Outline each blood parasite and name the species.
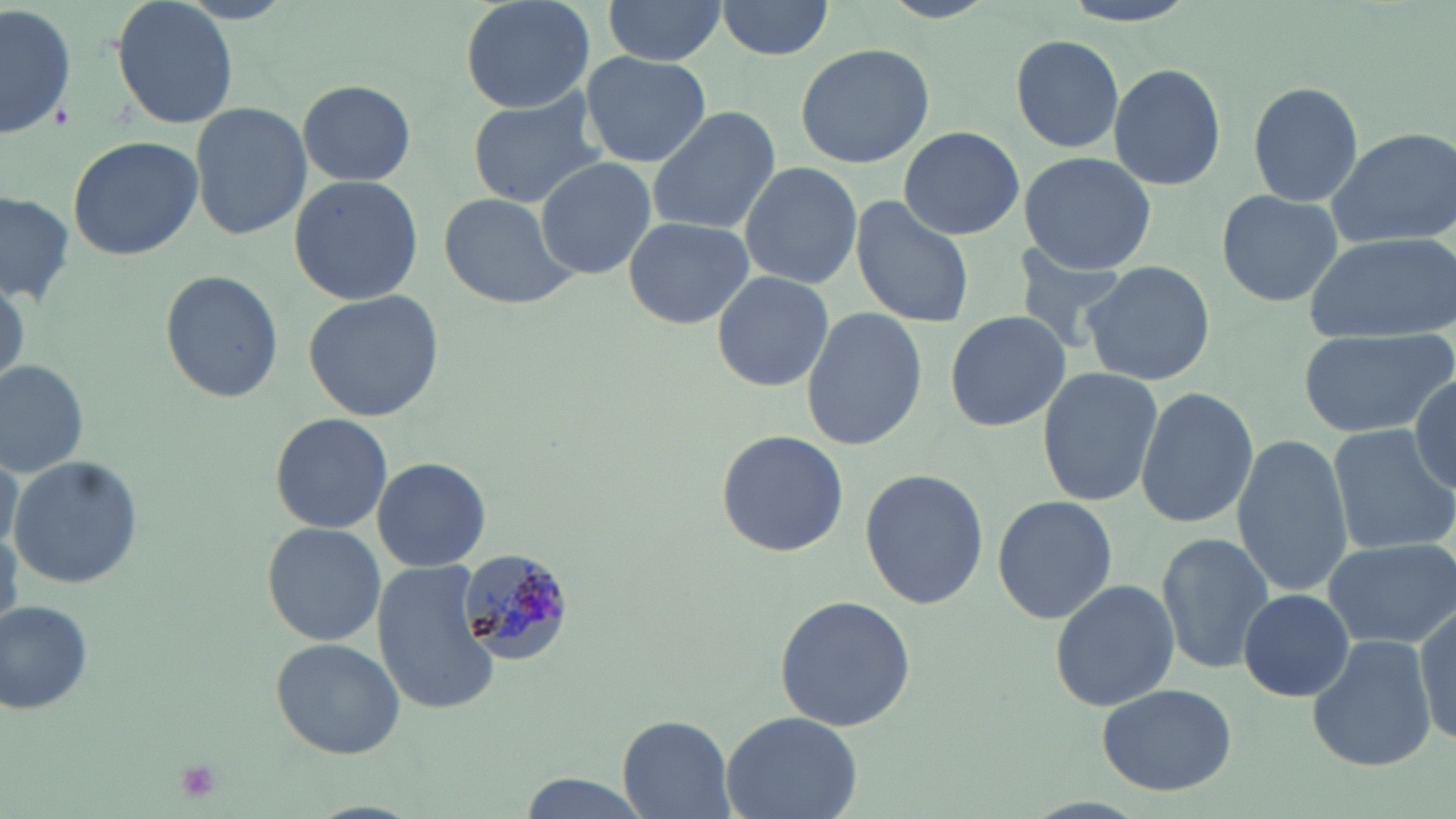

Approximate bounding boxes as [x1, y1, x2, y2] in pixels.
Plasmodium malariae-infected red blood cells: [463, 548, 574, 663].
No Plasmodium falciparum, Plasmodium ovale, Plasmodium vivax, Babesia divergens, or Trypanosoma brucei observed.

slide-level diagnosis = Plasmodium malariae
platelet locations = approximate bounding boxes as [x1, y1, x2, y2] in pixels: [174, 759, 222, 801]
stain = May-Grünwald-Giemsa
preparation = thin blood film
field of view = single
magnification = 1000x
uninfected red blood cell locations = approximate bounding boxes as [x1, y1, x2, y2] in pixels: [111, 0, 235, 129], [458, 0, 598, 114], [715, 0, 838, 58], [601, 1, 727, 67], [2, 2, 77, 145], [1009, 32, 1126, 155], [795, 42, 933, 169], [581, 50, 710, 168], [1106, 61, 1226, 191], [297, 78, 417, 186], [1246, 81, 1364, 207], [466, 94, 606, 208], [189, 99, 309, 242], [645, 105, 778, 235], [899, 125, 1024, 241], [1325, 128, 1456, 247], [66, 134, 203, 261], [1018, 150, 1155, 276], [535, 156, 657, 279], [737, 159, 862, 287], [288, 175, 425, 305], [1215, 188, 1344, 309], [1, 190, 74, 304], [439, 192, 580, 311], [852, 195, 976, 328], [621, 215, 755, 330], [1303, 230, 1455, 344], [1009, 246, 1133, 354], [1080, 260, 1214, 387], [159, 269, 285, 402], [711, 269, 835, 392], [303, 290, 447, 422], [801, 308, 927, 453], [944, 311, 1069, 432], [1300, 326, 1453, 440], [0, 359, 90, 479], [1036, 367, 1164, 509], [1412, 373, 1454, 495], [1135, 385, 1257, 529], [270, 412, 392, 534], [1329, 423, 1456, 555], [715, 428, 848, 557], [1231, 434, 1352, 597], [0, 451, 22, 555], [9, 456, 144, 588], [370, 456, 492, 573], [860, 466, 987, 611], [990, 496, 1118, 625], [261, 521, 386, 646], [1157, 532, 1274, 673], [1323, 538, 1456, 647], [373, 560, 500, 714], [1048, 576, 1179, 713], [1239, 588, 1354, 702], [773, 595, 916, 729], [2, 600, 97, 716], [1413, 600, 1455, 747], [1378, 616, 1456, 756], [1306, 634, 1435, 771], [269, 638, 405, 759], [1099, 684, 1240, 797], [720, 710, 863, 819], [619, 714, 737, 817]
modality = light microscopy
image size = 1456×819 pixels